Classify this cell by malaria status.
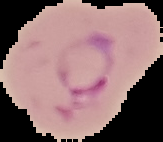

Parasitized.

Summary:
  - Preparation: thin blood smear
  - Image size: 163×142 pixels
  - Image type: segmented cell region on a black background